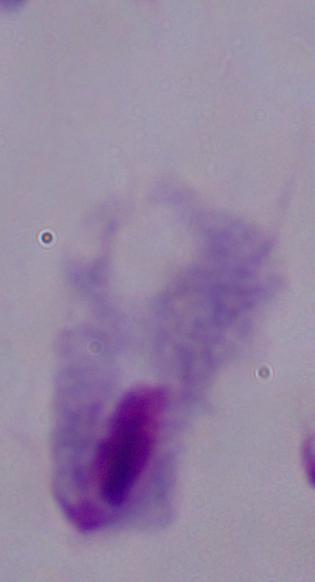
Summary:
  - Modality: photomicrograph
  - Magnification: 1000x
  - Identification: trichomonad